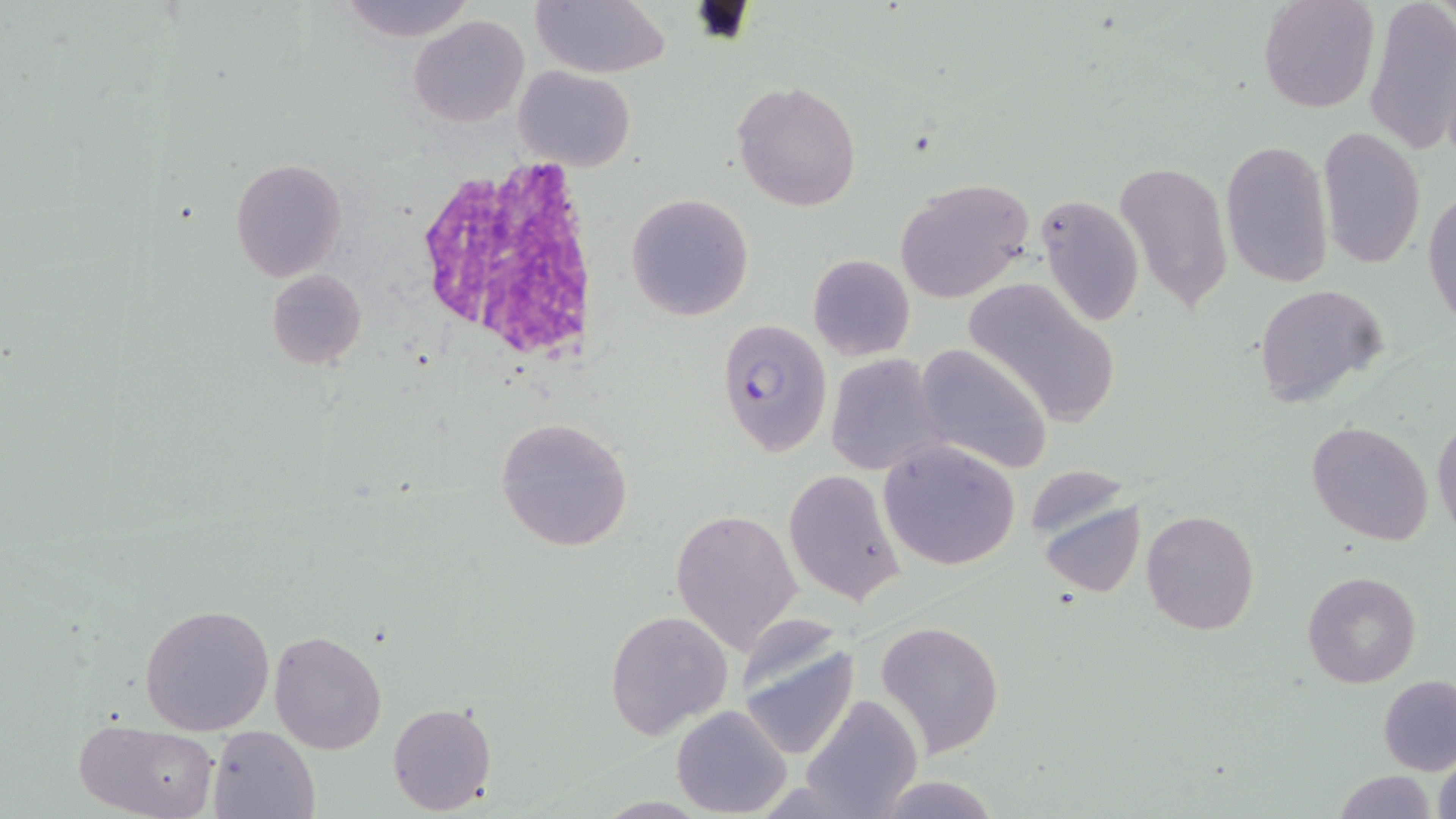
slide-level diagnosis = Plasmodium falciparum
field of view = single
magnification = 1000x
white blood cell locations = approximate bounding boxes as (x1,y1)-(x2,y2) corner pairs in pixels: (412,158)-(602,365)
image size = 1456×819 pixels
Plasmodium falciparum-infected red blood cell locations = approximate bounding boxes as (x1,y1)-(x2,y2) corner pairs in pixels: (715,318)-(832,454)
uninfected red blood cell locations = approximate bounding boxes as (x1,y1)-(x2,y2) corner pairs in pixels: (338,0)-(479,43), (1257,0)-(1379,115), (1363,0)-(1456,157), (530,1)-(670,79), (408,14)-(529,127), (513,65)-(636,171), (733,80)-(860,213), (1317,126)-(1427,270), (1220,138)-(1335,292), (228,157)-(347,283), (1114,161)-(1233,314), (896,176)-(1034,303), (1424,187)-(1456,331), (625,192)-(754,323), (1035,192)-(1145,330), (808,254)-(915,360), (266,269)-(366,370), (964,279)-(1122,428), (1251,284)-(1387,409), (914,342)-(1054,475), (825,354)-(943,476), (1431,413)-(1456,541), (495,417)-(633,551), (1306,420)-(1434,546), (878,440)-(1020,570), (783,469)-(907,605), (1038,496)-(1146,598), (670,507)-(803,653), (1140,509)-(1261,636), (1302,571)-(1422,689), (138,604)-(276,735), (605,608)-(733,738), (874,620)-(1004,757), (268,628)-(388,756), (736,635)-(857,764), (1377,676)-(1456,776), (801,694)-(923,819), (387,701)-(498,815), (671,703)-(793,817), (73,717)-(220,819), (207,724)-(323,819), (1430,745)-(1455,819), (1332,770)-(1438,819), (873,775)-(1002,817)
stain = May-Grünwald-Giemsa
preparation = thin blood film
modality = optical microscopy